Identify the blood parasite species.
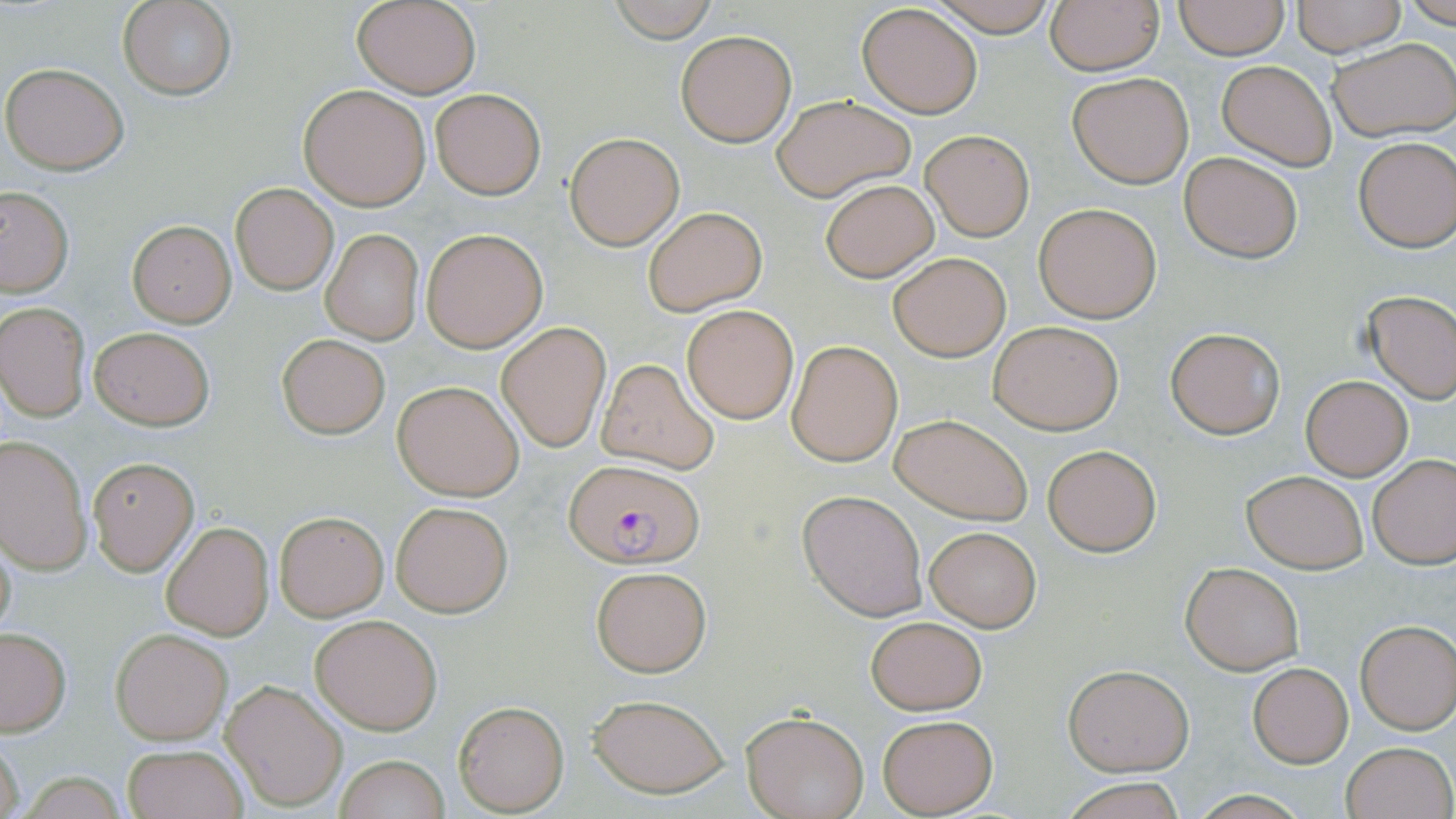

Plasmodium falciparum.

Summary:
  - Coordinate format: approximate bounding boxes as named x1/y1/x2/y2 corners in pixels
  - Plasmodium falciparum-infected red blood cell locations: (x1=562, y1=458, x2=702, y2=567)
  - Uninfected red blood cell locations: (x1=119, y1=0, x2=236, y2=100), (x1=352, y1=0, x2=481, y2=98), (x1=604, y1=0, x2=724, y2=43), (x1=925, y1=1, x2=1064, y2=35), (x1=1174, y1=1, x2=1288, y2=58), (x1=1291, y1=1, x2=1406, y2=55), (x1=1045, y1=2, x2=1163, y2=74), (x1=856, y1=4, x2=983, y2=119), (x1=675, y1=30, x2=796, y2=147), (x1=1327, y1=37, x2=1456, y2=142), (x1=1217, y1=60, x2=1336, y2=170), (x1=2, y1=62, x2=129, y2=174), (x1=1066, y1=71, x2=1195, y2=189), (x1=299, y1=84, x2=433, y2=211), (x1=431, y1=88, x2=545, y2=199), (x1=771, y1=94, x2=915, y2=200), (x1=919, y1=129, x2=1035, y2=241), (x1=565, y1=132, x2=685, y2=250), (x1=1353, y1=136, x2=1456, y2=251), (x1=1178, y1=150, x2=1303, y2=264), (x1=820, y1=178, x2=939, y2=283), (x1=231, y1=183, x2=338, y2=294), (x1=0, y1=187, x2=74, y2=297), (x1=1034, y1=201, x2=1162, y2=322), (x1=643, y1=207, x2=765, y2=315), (x1=127, y1=219, x2=236, y2=328), (x1=421, y1=227, x2=546, y2=352), (x1=321, y1=230, x2=423, y2=344), (x1=889, y1=252, x2=1009, y2=361), (x1=1362, y1=290, x2=1456, y2=403), (x1=0, y1=302, x2=92, y2=421), (x1=682, y1=305, x2=798, y2=422), (x1=989, y1=321, x2=1123, y2=434), (x1=497, y1=322, x2=611, y2=449), (x1=89, y1=326, x2=215, y2=431), (x1=1165, y1=328, x2=1283, y2=438), (x1=275, y1=333, x2=390, y2=439), (x1=787, y1=341, x2=901, y2=466), (x1=594, y1=357, x2=721, y2=473), (x1=1300, y1=376, x2=1412, y2=480), (x1=393, y1=380, x2=525, y2=500), (x1=891, y1=414, x2=1033, y2=524), (x1=1, y1=437, x2=93, y2=574), (x1=1041, y1=444, x2=1162, y2=555), (x1=1368, y1=455, x2=1456, y2=568), (x1=87, y1=457, x2=199, y2=575), (x1=1241, y1=470, x2=1369, y2=573), (x1=798, y1=491, x2=927, y2=619), (x1=391, y1=500, x2=512, y2=617), (x1=273, y1=509, x2=389, y2=620), (x1=160, y1=521, x2=273, y2=640), (x1=926, y1=527, x2=1040, y2=632), (x1=0, y1=528, x2=18, y2=646), (x1=1180, y1=562, x2=1304, y2=674), (x1=590, y1=565, x2=712, y2=677), (x1=309, y1=613, x2=442, y2=734), (x1=865, y1=616, x2=987, y2=714), (x1=1355, y1=620, x2=1456, y2=733), (x1=0, y1=628, x2=72, y2=736), (x1=111, y1=630, x2=231, y2=744), (x1=1247, y1=662, x2=1353, y2=767), (x1=1063, y1=664, x2=1193, y2=776), (x1=221, y1=680, x2=346, y2=811), (x1=586, y1=692, x2=732, y2=798), (x1=453, y1=701, x2=568, y2=815), (x1=743, y1=711, x2=869, y2=819), (x1=876, y1=713, x2=998, y2=816), (x1=1, y1=736, x2=26, y2=819), (x1=1340, y1=741, x2=1453, y2=819), (x1=122, y1=744, x2=249, y2=819), (x1=335, y1=754, x2=449, y2=819), (x1=1061, y1=776, x2=1187, y2=818)
  - Modality: light microscopy
  - Stain: May-Grünwald-Giemsa
  - Magnification: 1000x
  - Preparation: thin blood smear
  - Field of view: single
  - Image size: 1456×819 pixels